Describe the morphology of the red blood cells.
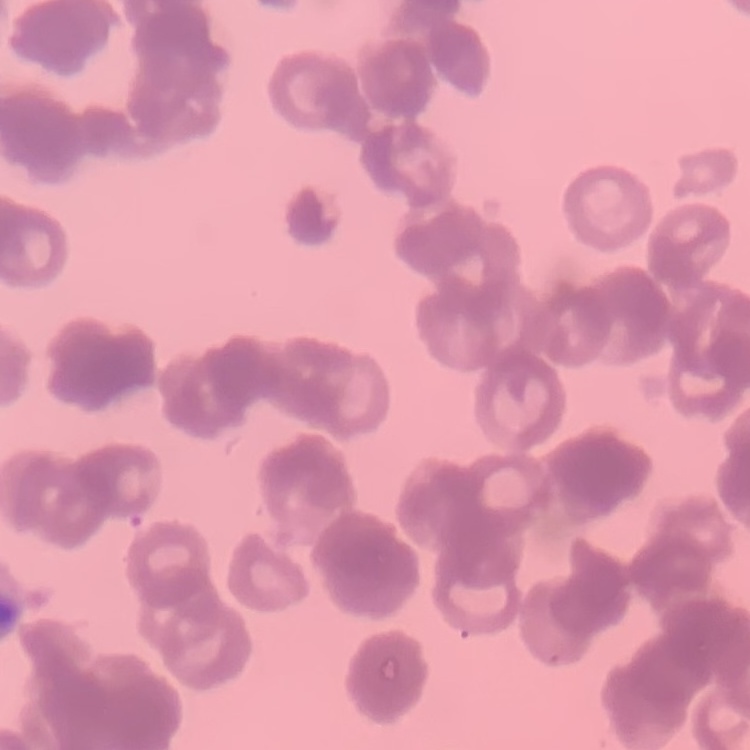
Rouleaux formation.

preparation = thin peripheral smear
image type = one tile cut from a larger photomicrograph
stain = Field's or Giemsa